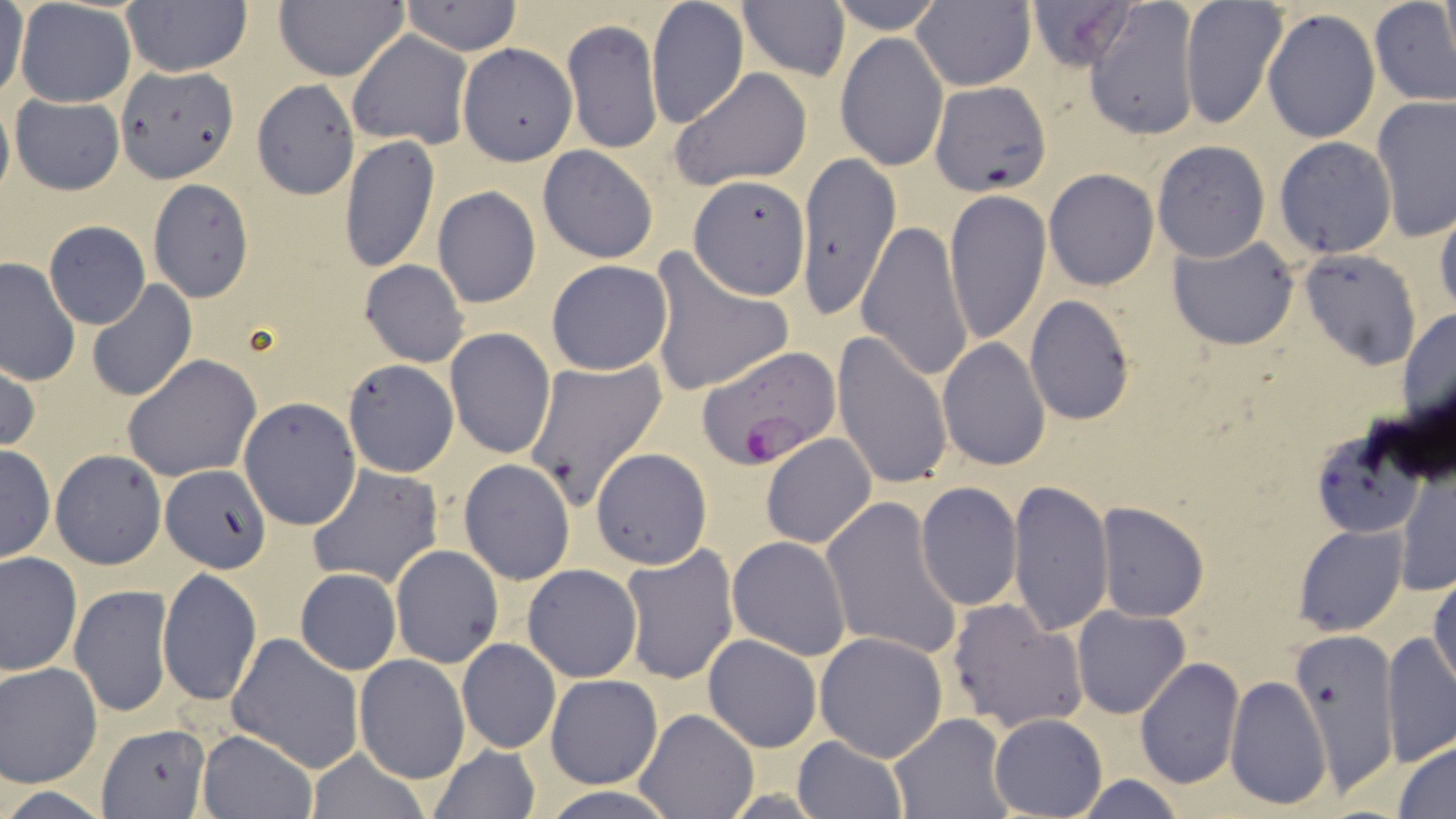

Approximate bounding boxes as (x1, y1, x2, y2) in pixels. Uninfected red blood cell locations: (15, 0, 136, 108), (273, 0, 407, 81), (826, 0, 946, 34), (912, 0, 1036, 92), (1023, 0, 1138, 72), (1178, 0, 1287, 130), (1439, 0, 1454, 75), (121, 1, 252, 76), (399, 1, 522, 55), (647, 1, 749, 129), (738, 1, 851, 82), (1084, 1, 1200, 140), (1369, 1, 1456, 109), (2, 2, 30, 107), (1262, 7, 1380, 144), (562, 19, 662, 154), (347, 30, 472, 149), (835, 33, 948, 171), (456, 43, 576, 165), (117, 65, 237, 182), (669, 67, 812, 191), (252, 80, 359, 201), (929, 80, 1052, 198), (0, 93, 14, 204), (10, 95, 125, 195), (1372, 98, 1455, 239), (338, 136, 440, 273), (1273, 137, 1396, 259), (1152, 140, 1269, 261), (537, 145, 658, 264), (798, 157, 903, 317), (1043, 168, 1160, 291), (688, 175, 808, 299), (147, 179, 254, 302), (433, 186, 542, 309), (945, 188, 1051, 347), (1433, 198, 1455, 322), (858, 218, 974, 381), (44, 221, 149, 330), (1166, 233, 1300, 351), (1300, 250, 1420, 370), (648, 253, 794, 399), (1, 257, 80, 386), (359, 259, 470, 367), (545, 260, 673, 375), (86, 280, 197, 402), (1025, 295, 1136, 426), (1398, 305, 1456, 436), (443, 328, 556, 461), (832, 329, 954, 491), (937, 338, 1050, 471), (122, 354, 260, 482), (1, 355, 40, 457), (341, 359, 459, 478), (523, 359, 667, 511), (238, 398, 361, 529), (1308, 424, 1435, 541), (761, 433, 877, 548), (0, 445, 54, 564), (591, 447, 711, 569), (49, 449, 167, 570), (458, 458, 576, 585), (305, 463, 444, 590), (1396, 466, 1454, 598), (160, 467, 271, 573), (1009, 479, 1114, 637), (915, 482, 1023, 611), (821, 496, 964, 662), (1096, 503, 1209, 620), (1294, 524, 1407, 636), (727, 536, 854, 660), (390, 545, 503, 666), (620, 547, 740, 685), (0, 552, 82, 677), (521, 564, 643, 683), (1430, 567, 1455, 694), (158, 568, 261, 706), (294, 568, 400, 675), (70, 584, 173, 718), (946, 599, 1087, 734), (1071, 606, 1190, 719), (1287, 624, 1400, 799), (814, 630, 948, 761), (1382, 631, 1455, 768), (227, 633, 366, 774), (702, 634, 822, 753), (457, 638, 561, 754), (353, 654, 469, 782), (1135, 658, 1245, 790), (0, 662, 103, 790), (1226, 674, 1331, 811), (546, 675, 662, 789), (635, 708, 760, 818), (889, 713, 1014, 819), (989, 713, 1107, 818), (97, 722, 208, 818), (197, 730, 315, 818), (793, 737, 906, 818), (1394, 738, 1456, 818), (304, 745, 433, 819), (426, 745, 543, 819), (1069, 775, 1185, 818), (536, 782, 677, 819). Plasmodium falciparum-infected red blood cell locations: (696, 344, 840, 469). Slide-level diagnosis: Plasmodium falciparum. Captured at 1000x magnification. Single field of view. May-Grünwald-Giemsa stain. Thin blood smear. Light microscopy. Image is 1456×819 pixels.